Report the malaria status of this cell.
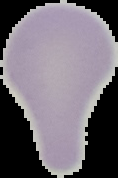

Uninfected.

From a thin blood film. Cell region segmented out of the field of view; the surrounding area is masked to black. Image is 118×178 pixels.